Classify this cell by malaria status.
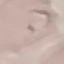

It is parasitized.

Summary:
  - Capture: smartphone through the microscope eyepiece
  - Stain: Giemsa
  - Preparation: thin smear
  - Image type: automatically extracted cell patch, resized to 64 × 64 pixels